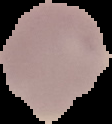 Malaria status: uninfected. From a thin blood film. Segmented cell region on a black background. Image is 112×124 pixels.